Report the malaria status of this cell.
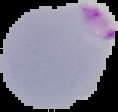

It is parasitized.

Summary:
  - Image size: 118×112 pixels
  - Image type: segmented cell region with the area outside set to black
  - Preparation: thin blood smear